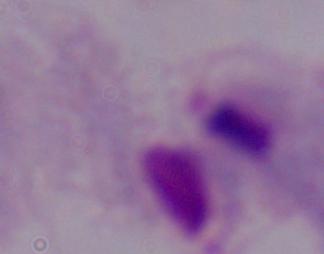
Summary:
  - Modality: photomicrograph
  - Identification: trichomonad
  - Magnification: 1000x